Assess this cell for malaria.
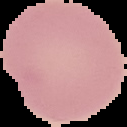
Uninfected.

preparation = thin blood smear
image size = 127×127 pixels
image type = segmented cell region on a black background